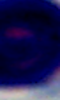 A leukocyte is shown. Micrograph. Captured at 1000x magnification.